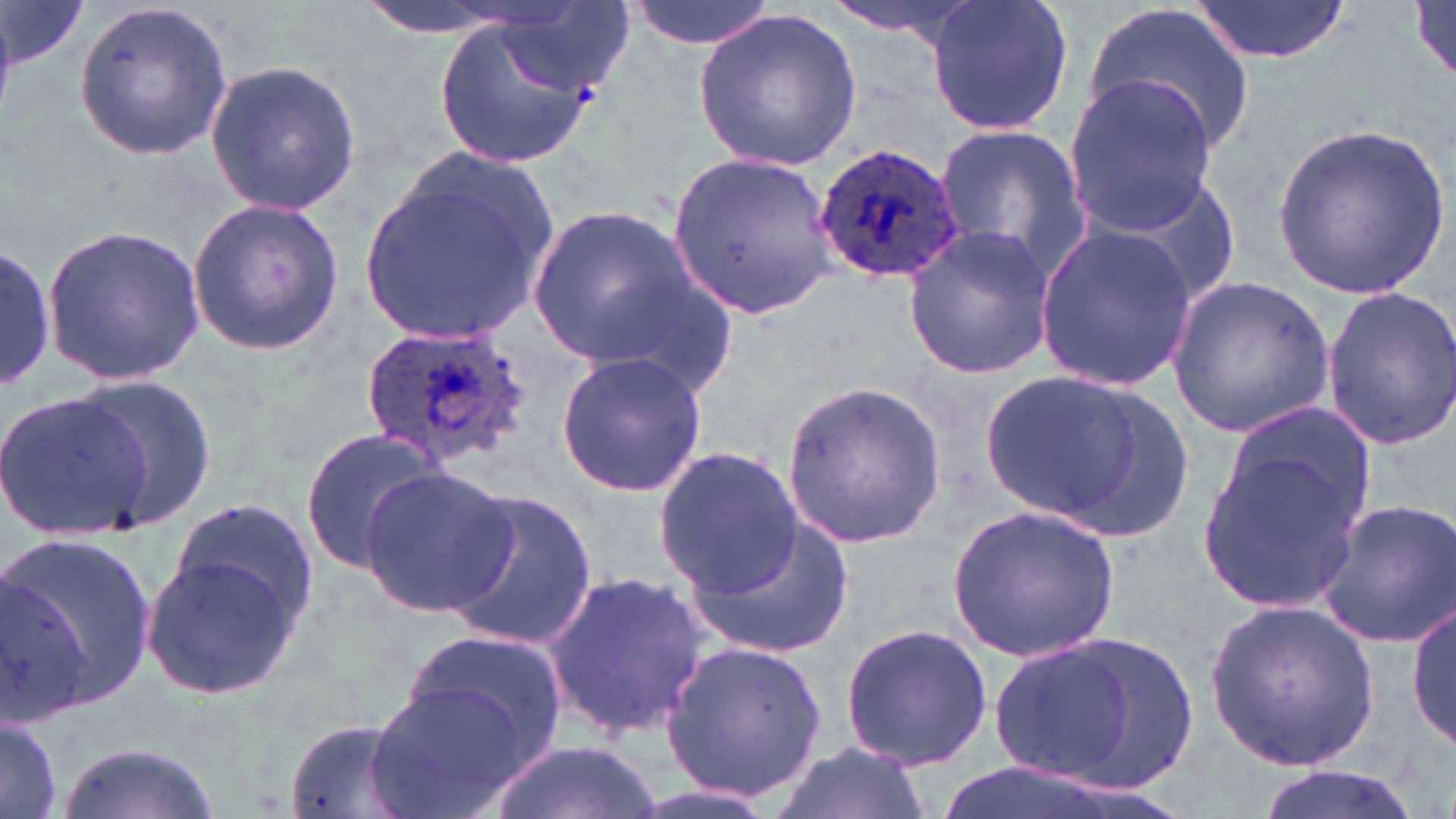 Approximate bounding boxes as [x1, y1, x2, y2] in pixels. Uninfected red blood cell locations: [2, 0, 87, 71], [353, 0, 527, 41], [623, 0, 784, 50], [824, 0, 985, 52], [923, 0, 1076, 138], [1187, 0, 1351, 65], [1412, 1, 1456, 81], [72, 2, 233, 161], [1086, 2, 1255, 157], [693, 8, 863, 170], [432, 9, 603, 166], [204, 59, 361, 217], [1062, 74, 1217, 231], [932, 122, 1091, 281], [1272, 123, 1448, 298], [665, 151, 840, 318], [358, 155, 562, 347], [1072, 167, 1240, 313], [186, 198, 345, 355], [525, 202, 701, 370], [41, 222, 207, 383], [903, 223, 1058, 380], [1032, 224, 1197, 393], [0, 238, 58, 396], [1168, 278, 1335, 437], [1322, 285, 1456, 447], [556, 352, 705, 496], [970, 363, 1169, 533], [70, 373, 219, 530], [780, 379, 947, 548], [0, 388, 154, 540], [1218, 406, 1377, 547], [300, 429, 447, 575], [1198, 442, 1367, 613], [654, 446, 805, 601], [361, 467, 515, 615], [440, 487, 595, 652], [1314, 496, 1456, 649], [170, 498, 323, 638], [949, 505, 1120, 661], [682, 509, 856, 661], [3, 530, 156, 711], [143, 546, 309, 702], [544, 571, 707, 739], [1409, 595, 1455, 757], [1206, 601, 1379, 771], [838, 622, 993, 771], [399, 626, 569, 766], [991, 637, 1145, 785], [658, 638, 830, 805], [367, 681, 530, 819], [0, 712, 65, 817], [276, 716, 427, 819], [490, 738, 661, 819], [768, 740, 929, 819], [56, 741, 222, 819], [1250, 766, 1430, 819], [619, 779, 784, 819]. Plasmodium ovale-infected red blood cell locations: [813, 143, 966, 285], [359, 324, 533, 472]. Slide-level diagnosis: Plasmodium ovale. One field of a larger specimen. Light microscopy. 1000x magnification. May-Grünwald-Giemsa stain. Thin blood film. Image is 1456×819 pixels.